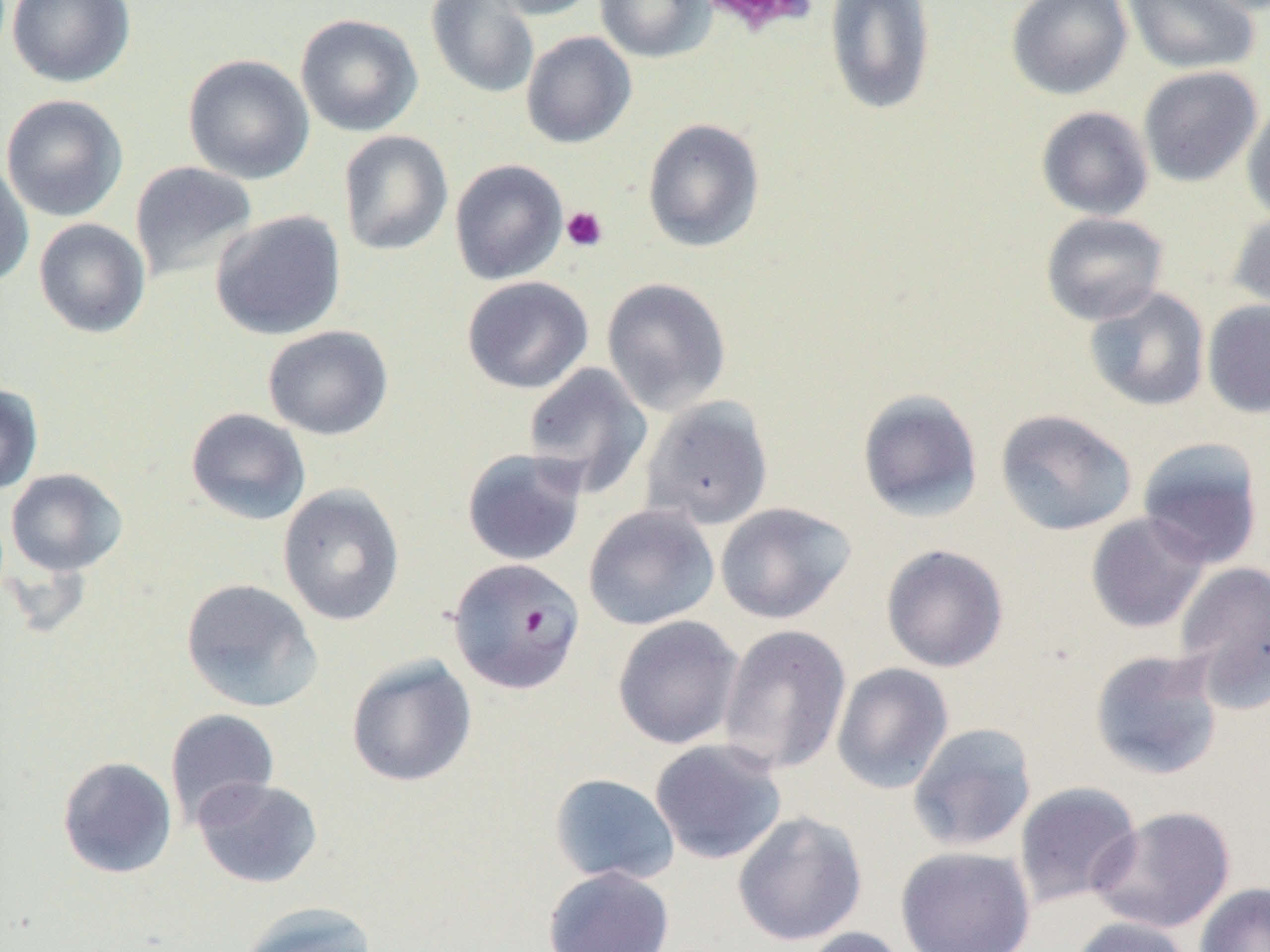 Approximate bounding boxes as (x1,y1)-(x2,y2) corner pairs in pixels. Uninfected red blood cell locations: (6,0)-(136,88), (425,0)-(540,100), (486,0)-(602,20), (594,0)-(716,63), (1006,0)-(1133,100), (1123,0)-(1261,75), (824,1)-(937,116), (295,14)-(423,137), (521,31)-(636,149), (183,54)-(315,184), (1138,66)-(1262,187), (1,94)-(129,222), (1241,100)-(1270,226), (1036,106)-(1154,221), (642,118)-(765,252), (338,130)-(454,256), (0,157)-(34,288), (450,158)-(569,285), (130,161)-(258,283), (210,210)-(347,340), (1227,210)-(1270,318), (1040,211)-(1169,325), (34,218)-(151,338), (461,276)-(593,394), (601,277)-(732,415), (1083,288)-(1211,412), (1202,300)-(1270,419), (262,325)-(393,440), (522,363)-(653,498), (0,382)-(44,495), (856,388)-(984,522), (641,396)-(774,530), (185,407)-(311,526), (995,408)-(1138,536), (1137,436)-(1265,568), (461,448)-(588,567), (6,468)-(127,576), (277,484)-(406,627), (714,502)-(856,624), (583,504)-(720,631), (1085,512)-(1211,633), (880,544)-(1009,672), (1174,561)-(1270,710), (180,578)-(323,713), (612,615)-(744,750), (718,624)-(852,775), (1089,648)-(1225,781), (345,654)-(477,788), (831,662)-(954,794), (165,708)-(280,827), (907,722)-(1038,852), (650,738)-(787,865), (57,756)-(178,879), (549,773)-(680,885), (192,777)-(323,889), (1013,781)-(1142,909), (1087,805)-(1237,934), (732,810)-(867,946), (895,845)-(1036,952), (542,865)-(675,952), (1194,882)-(1270,952), (236,902)-(379,952), (1067,916)-(1196,952), (798,926)-(912,952). Plasmodium falciparum-infected red blood cell locations: (447,558)-(585,694). Platelet locations: (698,0)-(819,36), (561,206)-(607,252). Slide-level diagnosis: Plasmodium falciparum. 1000x magnification. One field of a larger specimen. Optical microscopy. Image is 1270×952 pixels. Thin blood film.